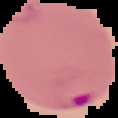 Malaria status: parasitized. Image is 118×118 pixels. From a thin blood smear. The area outside the segmented cell region is set to black.